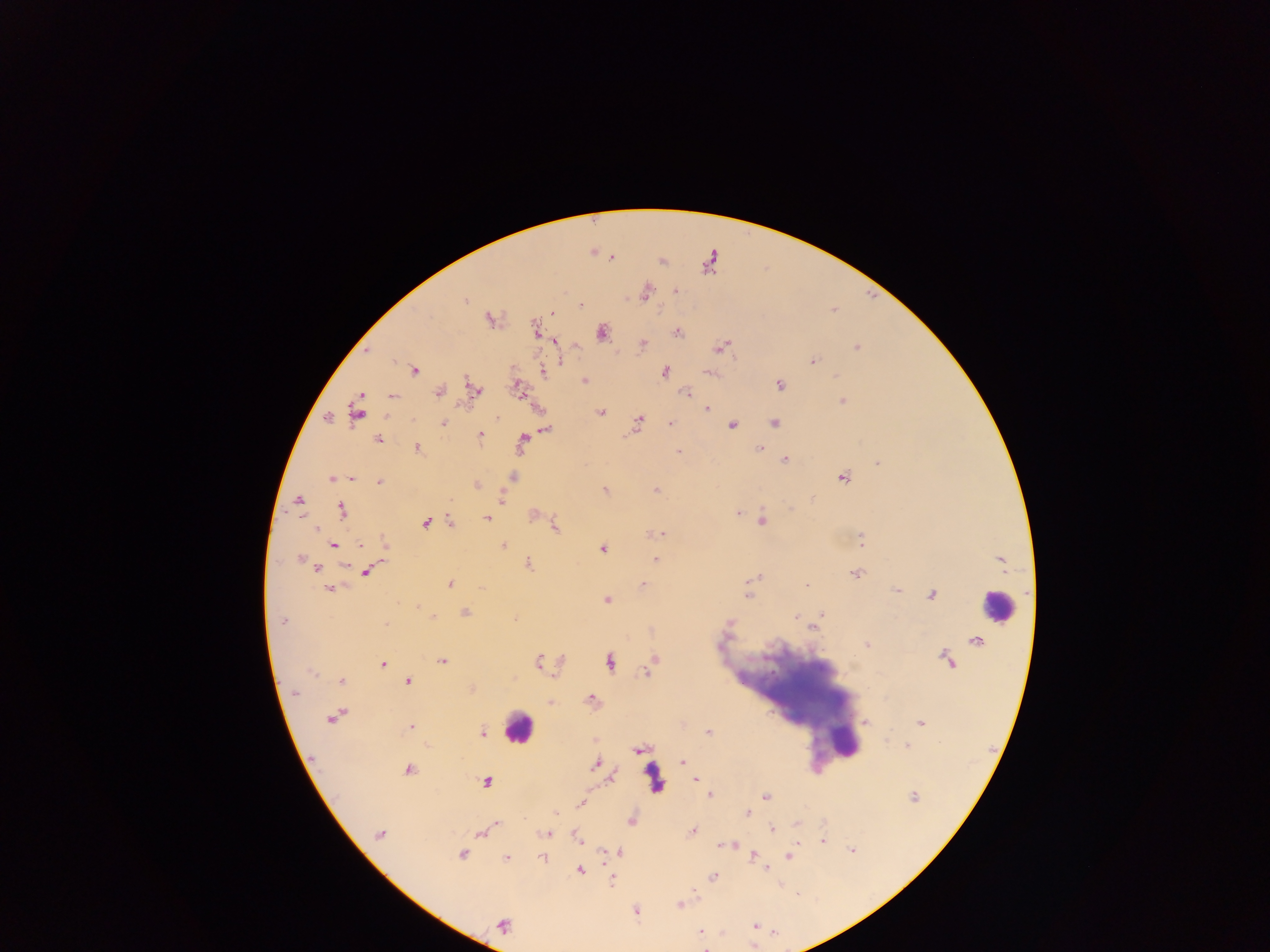

malaria_parasite_locations: 'approximate centers as {x, y} in pixels: {591, 251}, {612, 257}, {661, 260}, {676, 291}, {645, 292}, {464, 301}, {581, 305}, {551, 312}, {490, 319}, {534, 329}, {601, 332}, {677, 332}, {554, 340}, {641, 343}, {721, 346}, {856, 346}, {366, 350}, {811, 360}, {414, 369}, {542, 371}, {665, 372}, {709, 372}, {836, 376}, {584, 380}, {779, 385}, {517, 387}, {473, 389}, {684, 391}, {439, 392}, {360, 396}, {392, 396}, {842, 400}, {706, 408}, {356, 412}, {601, 412}, {496, 416}, {327, 418}, {638, 422}, {773, 422}, {443, 423}, {669, 423}, {731, 425}, {545, 428}, {479, 435}, {377, 439}, {521, 442}, {417, 447}, {676, 448}, {760, 449}, {679, 451}, {784, 460}, {878, 463}, {512, 477}, {332, 478}, {350, 478}, {842, 478}, {379, 482}, {476, 485}, {604, 490}, {655, 490}, {501, 498}, {298, 502}, {341, 510}, {739, 512}, {534, 515}, {486, 518}, {762, 520}, {450, 522}, {425, 523}, {555, 526}, {315, 528}, {652, 533}, {661, 533}, {861, 539}, {360, 544}, {384, 544}, {332, 545}, {503, 545}, {602, 548}, {300, 558}, {655, 559}, {1000, 560}, {527, 563}, {316, 567}, {365, 572}, {856, 573}, {750, 581}, {449, 583}, {643, 585}, {806, 585}, {481, 586}, {329, 588}, {750, 588}, {896, 590}, {932, 594}, {606, 599}, {416, 605}, {821, 612}, {464, 613}, {433, 616}, {796, 616}, {513, 618}, {281, 621}, {728, 622}, {812, 626}, {977, 640}, {867, 644}, {441, 660}, {653, 660}, {948, 660}, {538, 661}, {609, 661}, {382, 663}, {647, 672}, {340, 680}, {407, 680}, {471, 689}, {294, 692}, {591, 699}, {551, 702}, {333, 715}, {865, 723}, {921, 723}, {682, 724}, {410, 727}, {481, 732}, {713, 736}, {593, 741}, {907, 745}, {640, 749}, {682, 762}, {596, 763}, {408, 770}, {611, 778}, {695, 780}, {487, 781}, {710, 795}, {765, 796}, {914, 796}, {581, 804}, {554, 813}, {747, 813}, {631, 820}, {495, 824}, {797, 824}, {772, 829}, {693, 830}, {482, 832}, {379, 834}, {546, 834}, {577, 838}, {822, 840}, {725, 844}, {733, 844}, {852, 850}, {618, 851}, {462, 854}, {752, 855}, {789, 856}, {542, 857}, {506, 858}, {766, 867}, {579, 869}, {713, 877}, {612, 879}, {779, 884}, {678, 905}, {635, 911}, {503, 924}, {755, 925}, {701, 933}'
preparation: thick blood film
capture: mobile-phone photograph through a microscope
image_size: 1270×952 pixels
leukocyte_locations: 'approximate centers as {x, y} in pixels: {998, 606}, {518, 727}, {844, 742}, {653, 778}'
field_of_view: single
country: Ghana